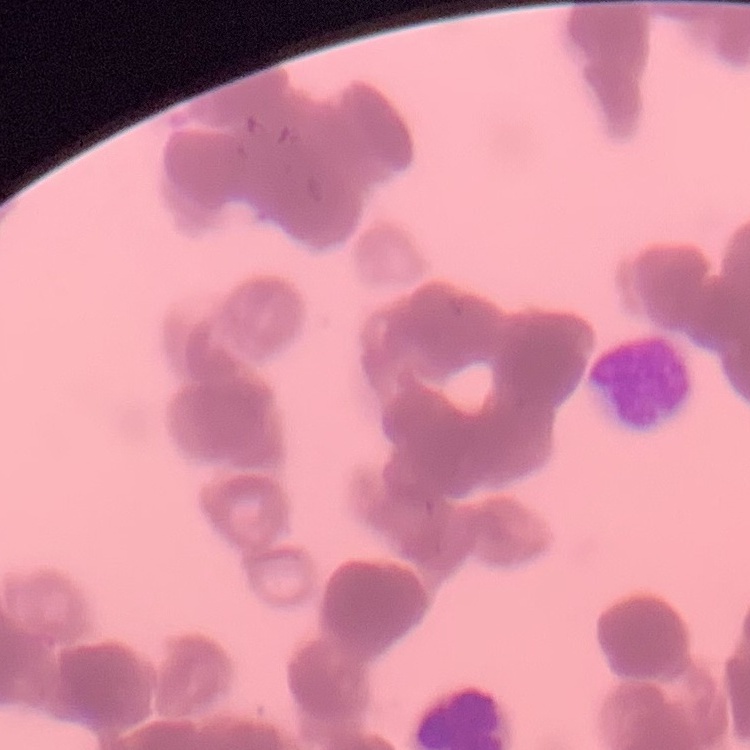
erythrocyte morphology = rouleaux formation
image type = square crop of a larger photomicrograph
preparation = thin blood film
stain = Field's or Giemsa